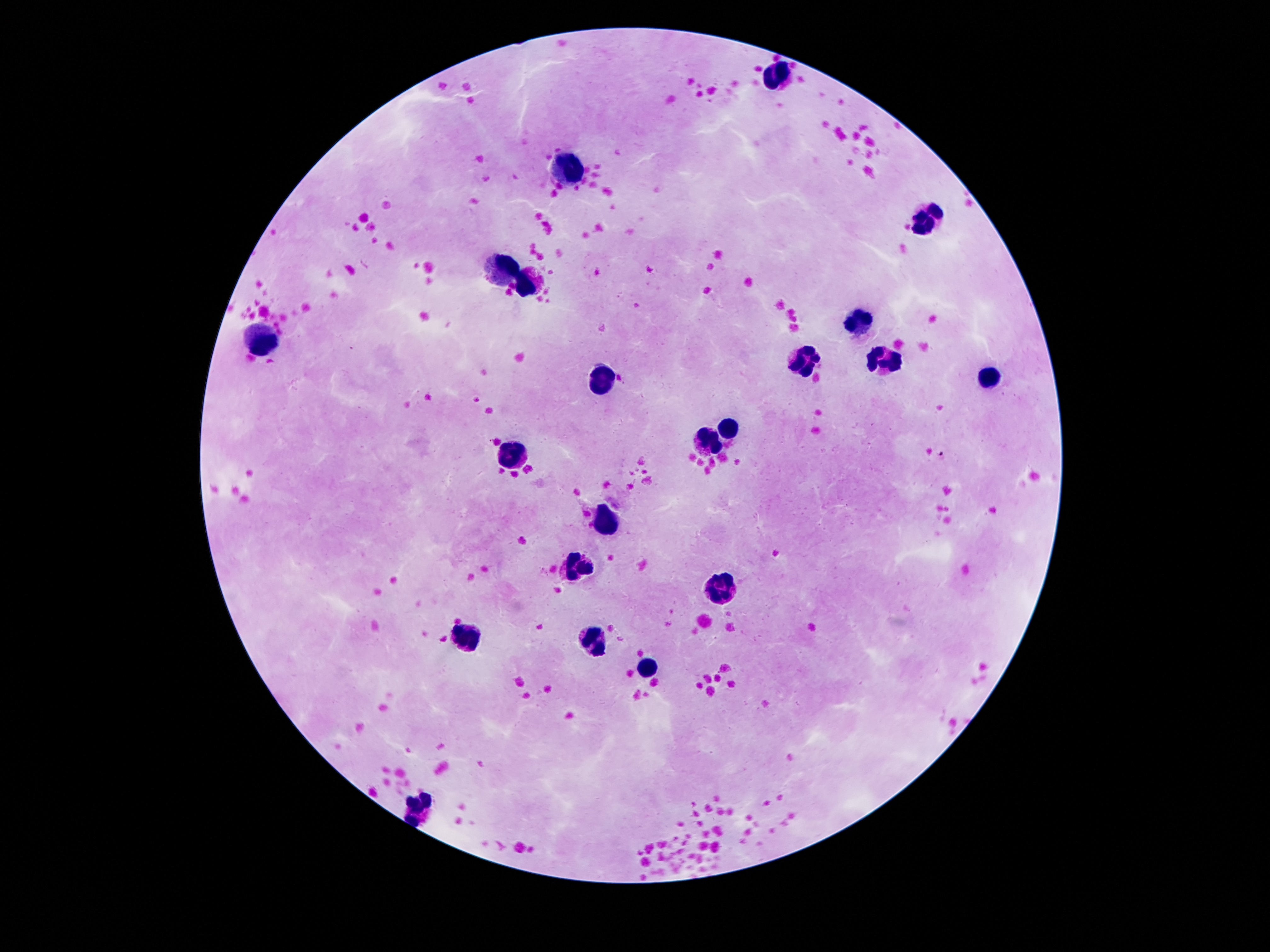
magnification: 100x
field_of_view: single
stain: Giemsa
preparation: thick blood film
leukocyte_locations: 'approximate centers as (x, y) in pixels: (774, 75), (567, 169), (924, 220), (504, 274), (530, 285), (860, 325), (264, 342), (886, 362), (804, 366), (987, 380), (600, 381), (732, 427), (709, 444), (516, 457), (607, 523), (579, 565), (718, 591), (467, 640), (592, 642), (648, 671), (420, 807)'
patient_malaria_status: negative
image_size: 1270×952 pixels
capture: smartphone camera through the microscope eyepiece